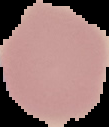
result: no Plasmodium parasites seen
preparation: thin blood smear
image_type: cell region segmented out of the field of view; surrounding area masked to black
image_size: 109×127 pixels